Report the malaria status of this cell.
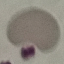
Uninfected.

Giemsa stain. Automatically extracted cell patch, resized to 64 × 64 pixels. Thin blood film. Acquired by smartphone through the microscope eyepiece.